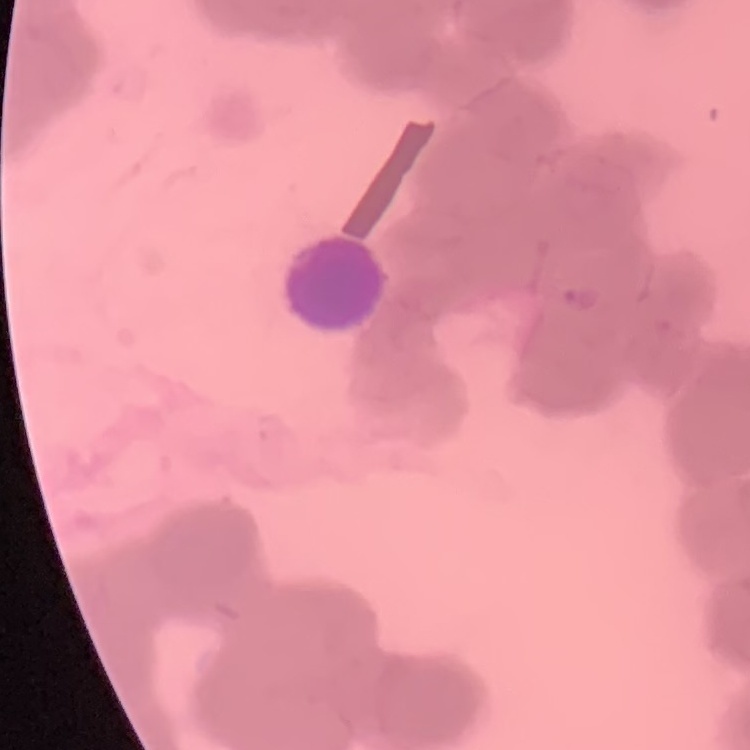

Summary:
  - Red blood cell morphology: rouleaux formation
  - Stain: Field's or Giemsa
  - Preparation: thin blood smear
  - Image type: square crop of a larger photomicrograph